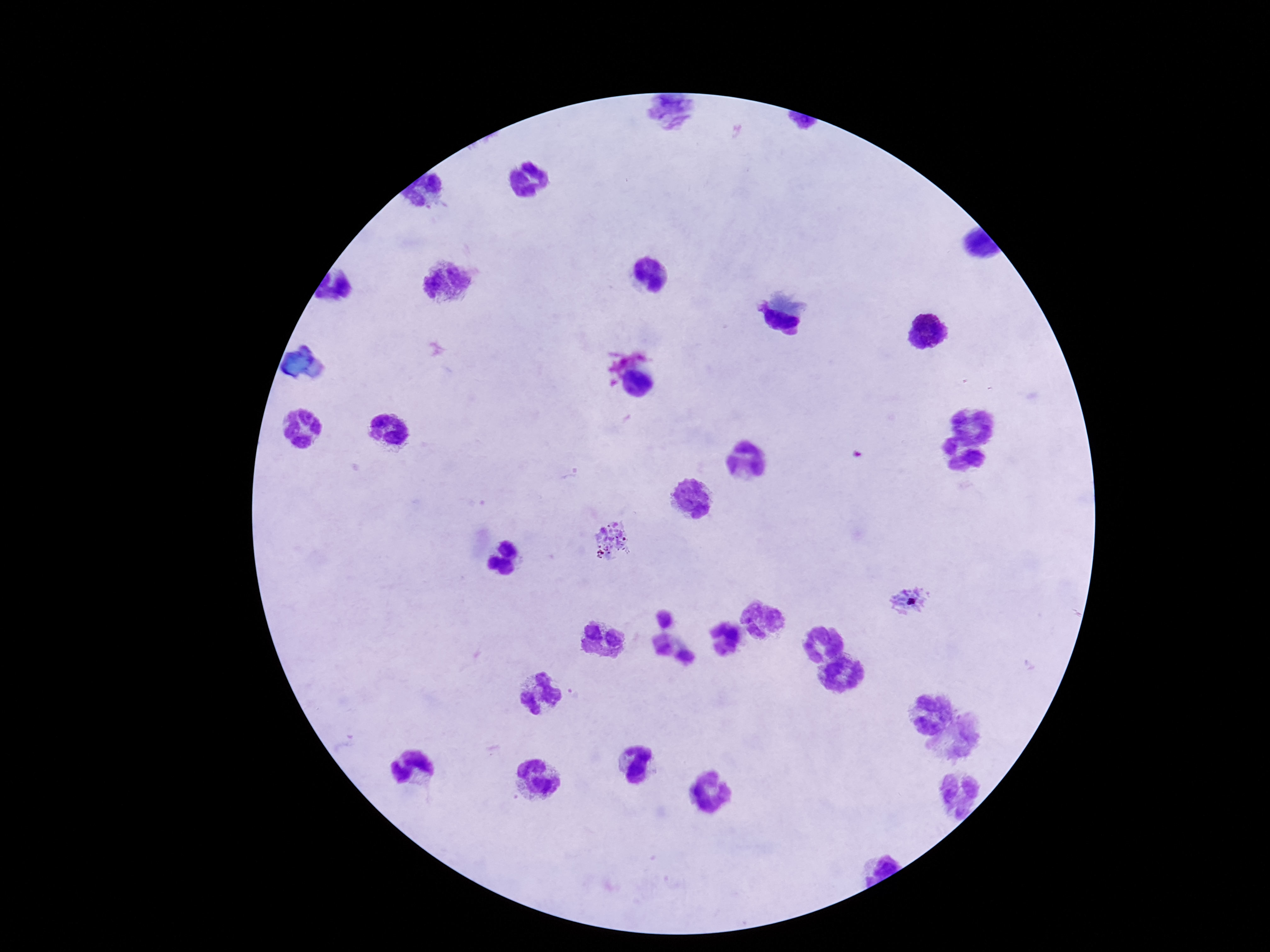 Approximate centers as [x, y] in pixels. Plasmodium parasite locations: [612, 540], [912, 601]. 100x magnification. Photographed through the microscope eyepiece with a smartphone camera. Giemsa-stained preparation. Image is 1270×952 pixels. Patient malaria status: infected. Thick peripheral-blood smear. One field from this slide.